Outline platelets.
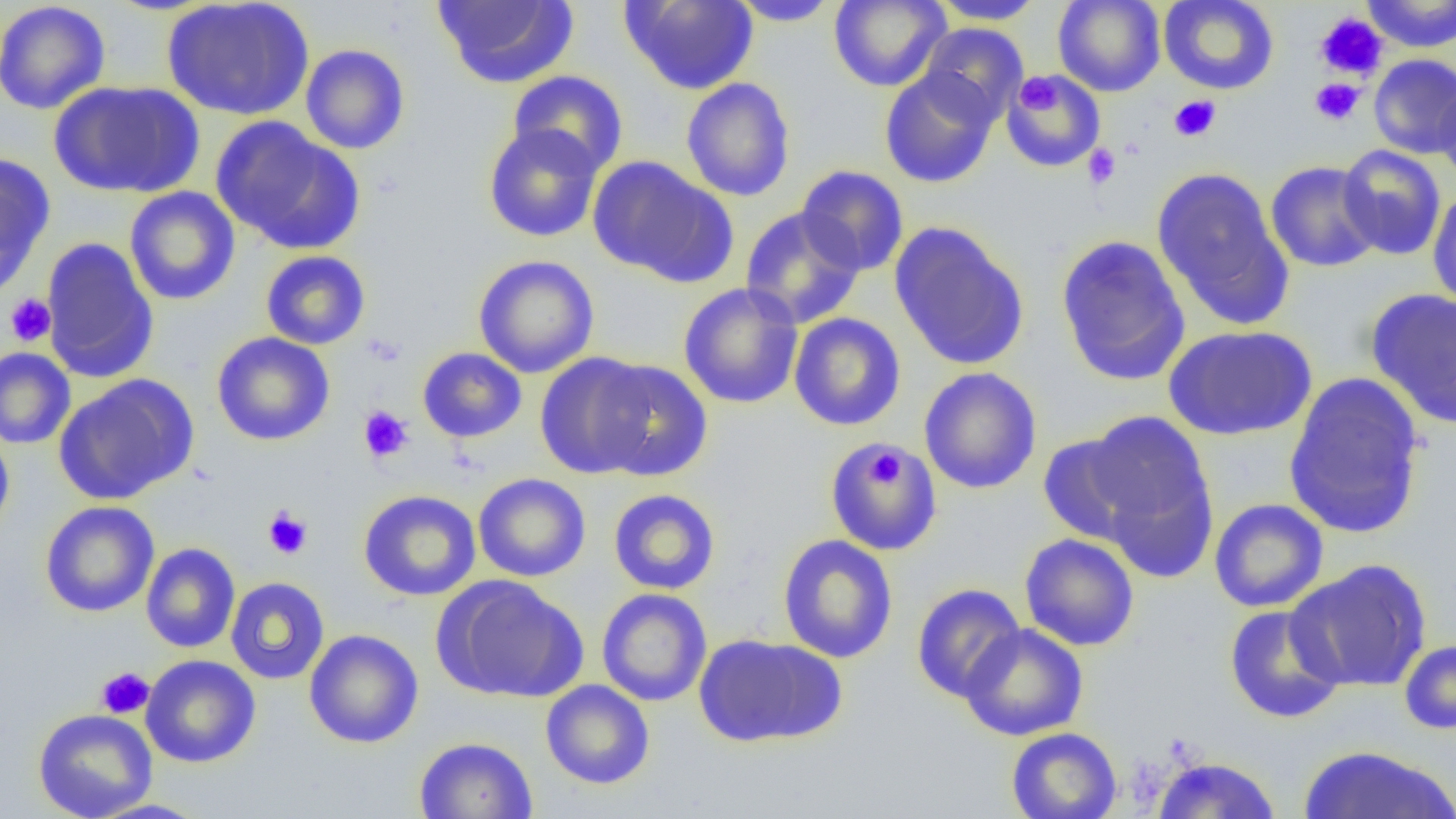
Approximate bounding boxes as (x1, y1, x2, y2) in pixels.
Platelets: (1315, 12, 1387, 80), (1017, 73, 1059, 115), (1309, 78, 1365, 126), (1169, 95, 1221, 142), (1082, 143, 1122, 190), (5, 294, 57, 346), (363, 333, 405, 367), (358, 406, 414, 463), (867, 443, 907, 490), (262, 506, 312, 559), (96, 667, 154, 719).

Summary:
  - Uninfected red blood cell locations: (0, 0, 111, 115), (161, 0, 315, 121), (433, 0, 578, 89), (729, 0, 841, 26), (929, 0, 1047, 25), (1053, 0, 1165, 96), (1158, 0, 1279, 94), (1361, 0, 1455, 52), (621, 1, 758, 94), (829, 1, 951, 92), (917, 22, 1028, 123), (300, 44, 410, 154), (1368, 53, 1456, 159), (879, 67, 1000, 188), (1002, 69, 1105, 172), (508, 70, 629, 176), (680, 77, 796, 202), (49, 80, 204, 198), (1434, 81, 1455, 189), (211, 116, 364, 255), (483, 123, 604, 242), (1337, 144, 1447, 260), (0, 152, 55, 294), (588, 156, 735, 286), (1265, 160, 1383, 273), (796, 165, 909, 276), (1151, 167, 1294, 330), (124, 186, 241, 305), (1426, 188, 1456, 311), (740, 206, 865, 329), (888, 222, 1030, 371), (1055, 234, 1192, 386), (41, 237, 159, 382), (260, 250, 370, 350), (473, 254, 599, 378), (678, 283, 804, 409), (1366, 289, 1456, 429), (789, 312, 906, 431), (1163, 324, 1318, 442), (211, 332, 335, 446), (0, 347, 76, 449), (417, 347, 527, 443), (535, 352, 658, 479), (590, 359, 714, 482), (919, 367, 1042, 494), (1284, 371, 1426, 540), (54, 374, 197, 505), (1083, 410, 1215, 549), (0, 429, 15, 538), (1037, 433, 1149, 546), (824, 440, 942, 556), (1103, 460, 1218, 586), (473, 473, 591, 582), (358, 489, 482, 601), (607, 489, 721, 595), (1209, 498, 1328, 612), (40, 500, 160, 617), (1019, 533, 1140, 651), (777, 534, 898, 663), (140, 542, 241, 653), (1287, 559, 1432, 693), (436, 576, 587, 703), (225, 577, 330, 685), (911, 583, 1025, 703), (597, 588, 712, 706), (1223, 604, 1346, 723), (959, 623, 1089, 741), (303, 629, 423, 748), (692, 633, 845, 748), (1398, 638, 1456, 734), (141, 654, 261, 768), (540, 679, 655, 789), (32, 708, 158, 819), (1005, 727, 1122, 819), (413, 736, 538, 818), (1296, 744, 1455, 819), (1151, 755, 1282, 818), (85, 798, 214, 819)
  - Slide-level diagnosis: no evidence of blood parasites
  - Modality: optical microscopy
  - Image size: 1456×819 pixels
  - Magnification: 1000x
  - Preparation: thin blood film
  - Field of view: one of a larger specimen